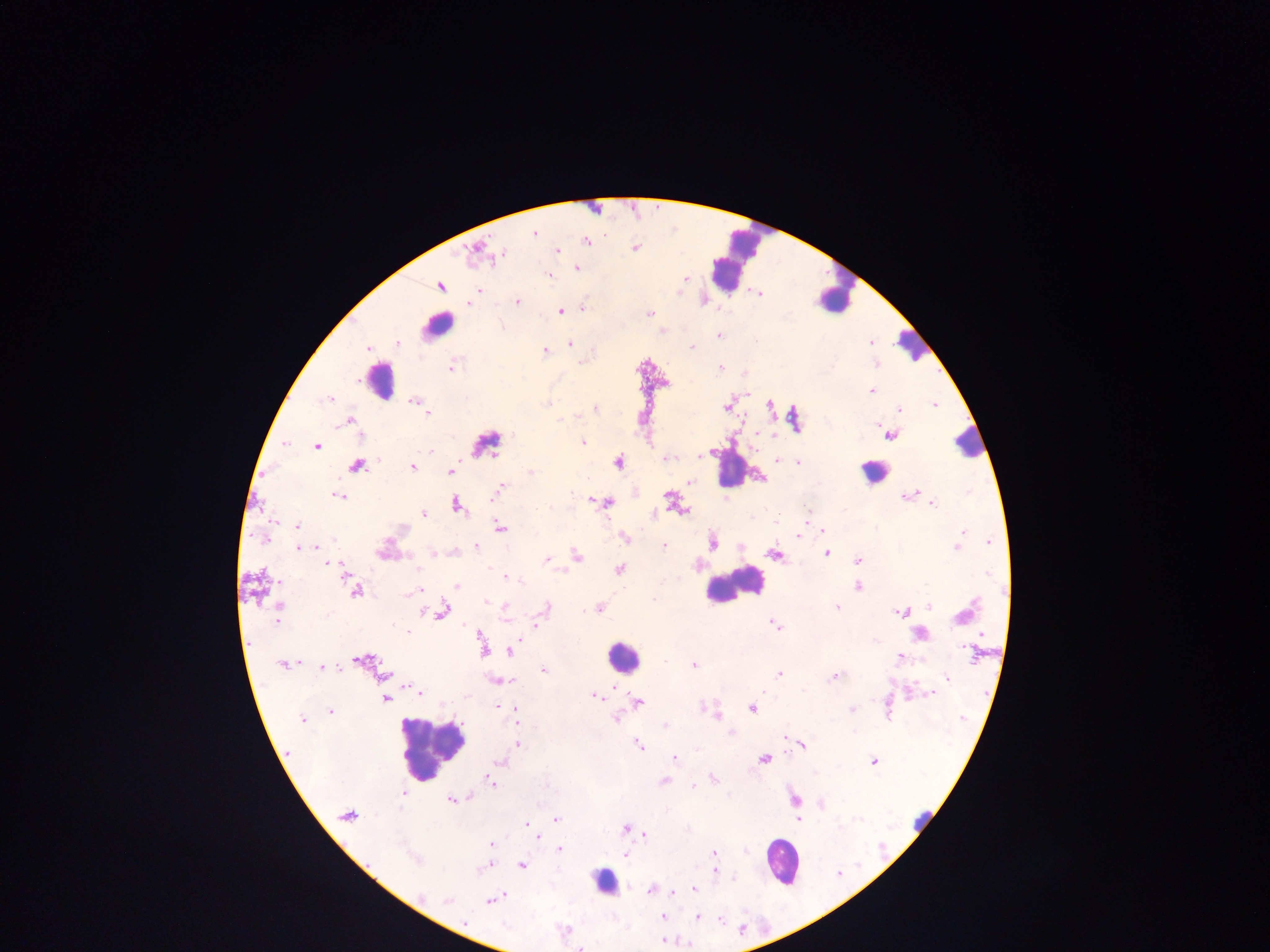

{
  "capture": "mobile-phone photograph through a microscope",
  "leukocyte_locations": "approximate centers as x y in pixels (subset; some below the resolvable size): 734 260; 837 298; 436 326; 913 345; 378 380; 969 443; 729 468; 873 472; 733 586; 622 657; 430 748; 923 815; 780 860; 604 881",
  "image_size": "1270×952 pixels",
  "field_of_view": "single",
  "country": "Ghana",
  "preparation": "thick blood film",
  "plasmodium_parasite_locations": "approximate centers as x y in pixels: 534 233; 587 241; 635 247; 475 248; 558 251; 502 256; 577 268; 548 275; 685 278; 440 286; 477 291; 759 294; 470 302; 517 302; 583 307; 561 311; 649 313; 718 335; 397 343; 570 343; 871 343; 692 347; 367 349; 545 350; 721 366; 452 367; 872 391; 330 398; 413 400; 547 404; 769 405; 935 405; 726 407; 596 409; 899 410; 427 414; 350 420; 559 420; 877 423; 891 435; 583 442; 486 443; 316 446; 430 451; 665 458; 776 461; 619 462; 798 462; 357 466; 412 466; 449 472; 530 472; 761 478; 690 483; 500 488; 913 493; 669 496; 907 496; 339 497; 493 497; 605 502; 933 503; 458 506; 683 510; 423 514; 806 518; 775 523; 297 526; 500 527; 823 531; 963 531; 799 536; 624 538; 265 539; 959 540; 990 541; 712 543; 664 546; 299 547; 476 547; 957 547; 316 548; 827 553; 434 554; 774 555; 577 557; 546 559; 857 561; 328 563; 619 569; 345 570; 987 572; 506 579; 518 581; 457 587; 857 587; 355 591; 417 591; 412 592; 486 602; 929 606; 837 607; 280 608; 546 608; 599 608; 442 610; 504 610; 424 612; 901 612; 961 616; 505 618; 277 619; 774 624; 536 625; 406 631; 482 647; 510 650; 972 654; 899 657; 364 661; 665 661; 282 665; 694 665; 323 667; 544 670; 383 675; 779 675; 835 677; 946 677; 502 681; 511 681; 417 691; 764 691; 931 694; 595 696; 385 699; 638 702; 497 707; 751 708; 852 709; 707 710; 330 712; 516 712; 716 712; 302 718; 616 719; 517 721; 665 726; 731 733; 784 737; 519 745; 803 745; 638 746; 674 758; 764 759; 501 762; 873 762; 714 779; 663 781; 491 782; 696 784; 693 786; 402 794; 471 798; 451 799; 794 799; 822 804; 347 816; 556 818; 798 819; 527 824; 625 828; 645 835; 535 838; 491 844; 560 849; 714 853; 626 855; 415 859; 488 865; 522 865; 734 878; 694 890; 650 891; 672 893; 490 900; 448 901; 662 917; 698 918; 719 919; 465 922; 664 941; 581 948"
}